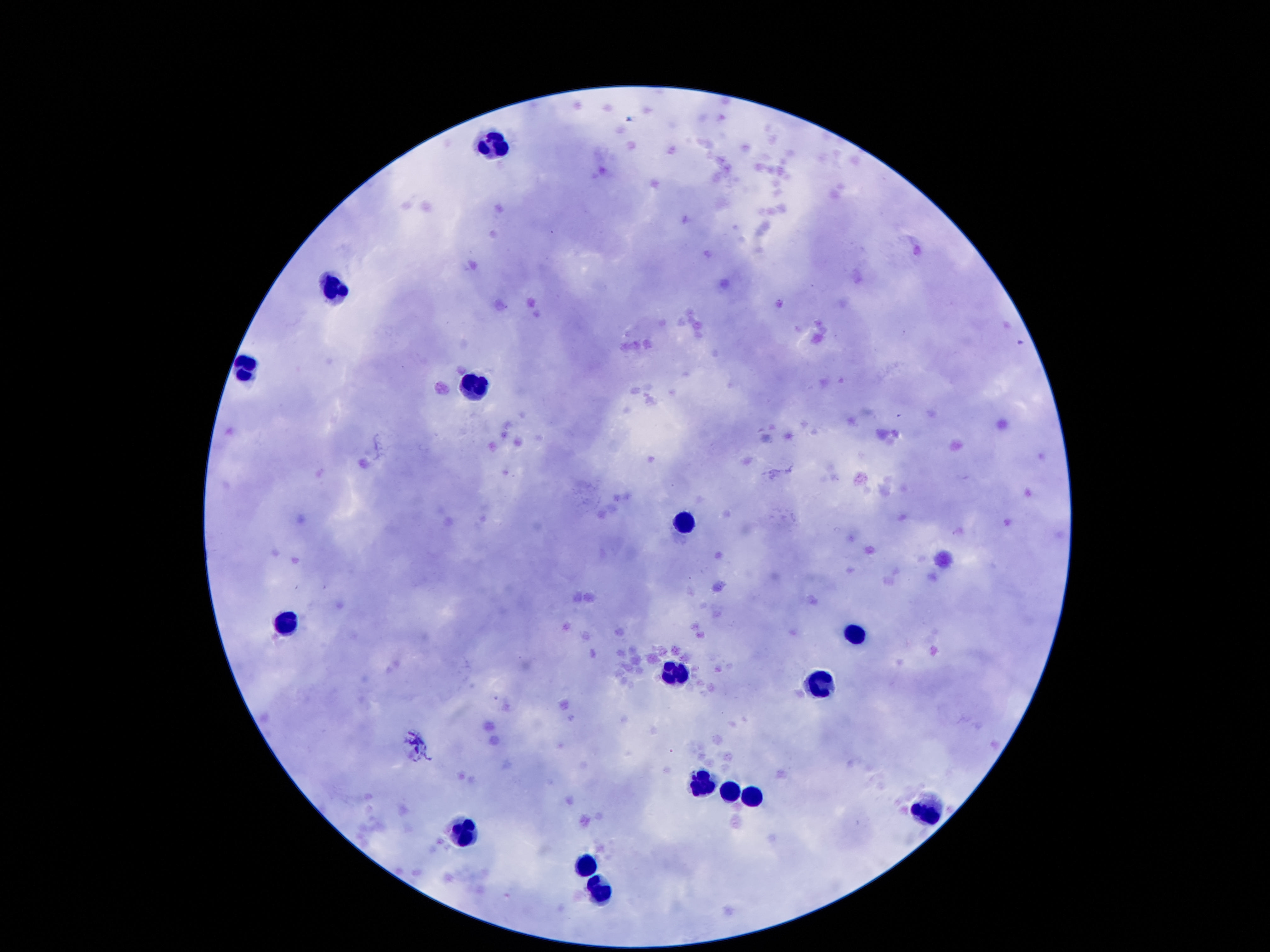
capture: smartphone camera through the microscope eyepiece
image_size: 1270×952 pixels
field_of_view: one from this slide
leukocyte_locations: 'approximate centers as (x, y) in pixels: (490, 142), (336, 289), (246, 369), (475, 381), (679, 522), (288, 617), (855, 631), (677, 671), (822, 684), (704, 783), (731, 791), (754, 793), (931, 806), (458, 829), (586, 862), (597, 886)'
patient_malaria_status: uninfected
preparation: thick blood smear
magnification: 100x
stain: Giemsa